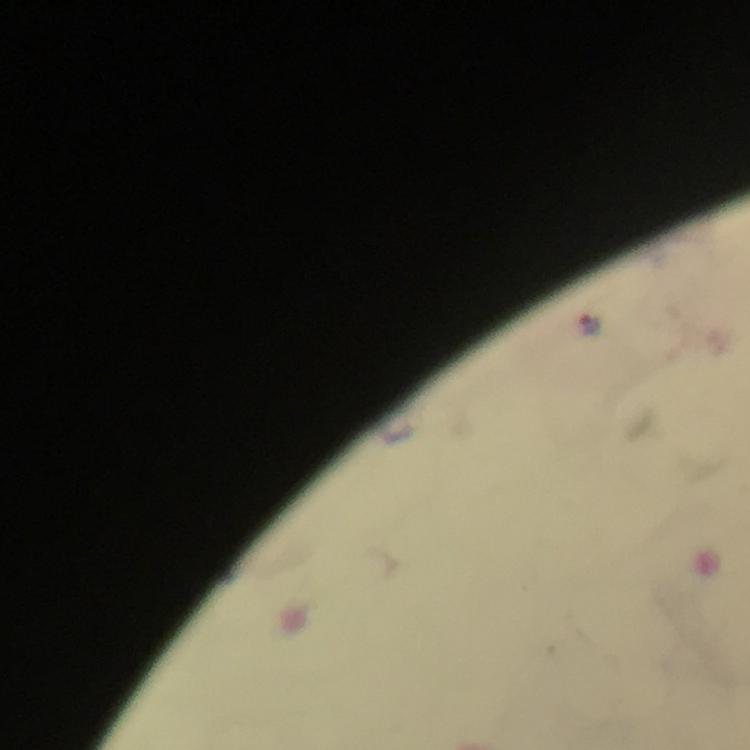
Approximate object centers, in pixels from the top-left corner.
Summary:
  - Malaria parasite locations: (x=591, y=322)
  - Cropped from: a single field of view
  - Immersion oil: applied
  - Stain: Giemsa
  - Image size: 750×750 pixels
  - Capture: smartphone mounted on the microscope
  - Context: from a diagnostic examination for malaria
  - Preparation: thick blood smear
  - Magnification: 100x